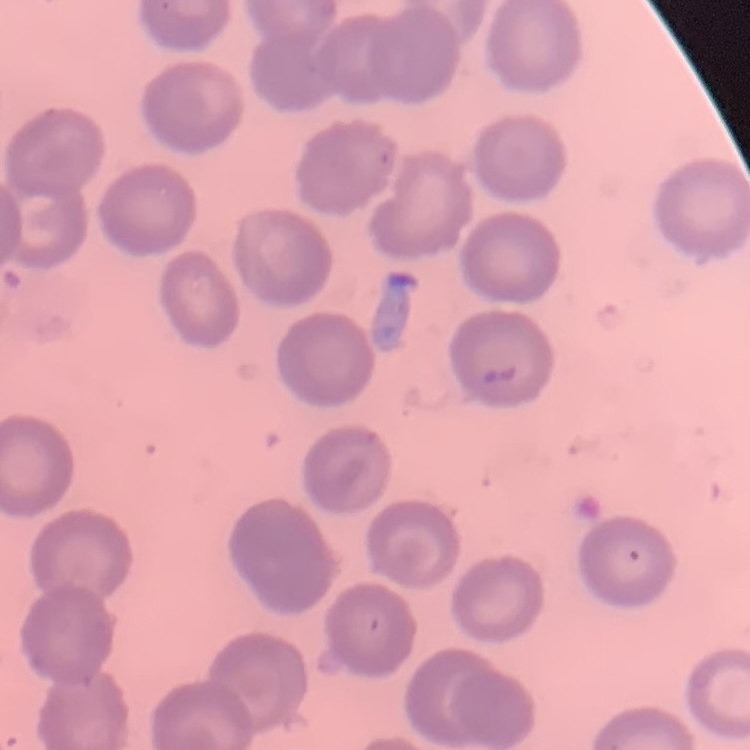 The red blood cells show no rouleaux formation. Square crop of a larger photomicrograph. Thin blood film. Stained with either Field's or Giemsa.